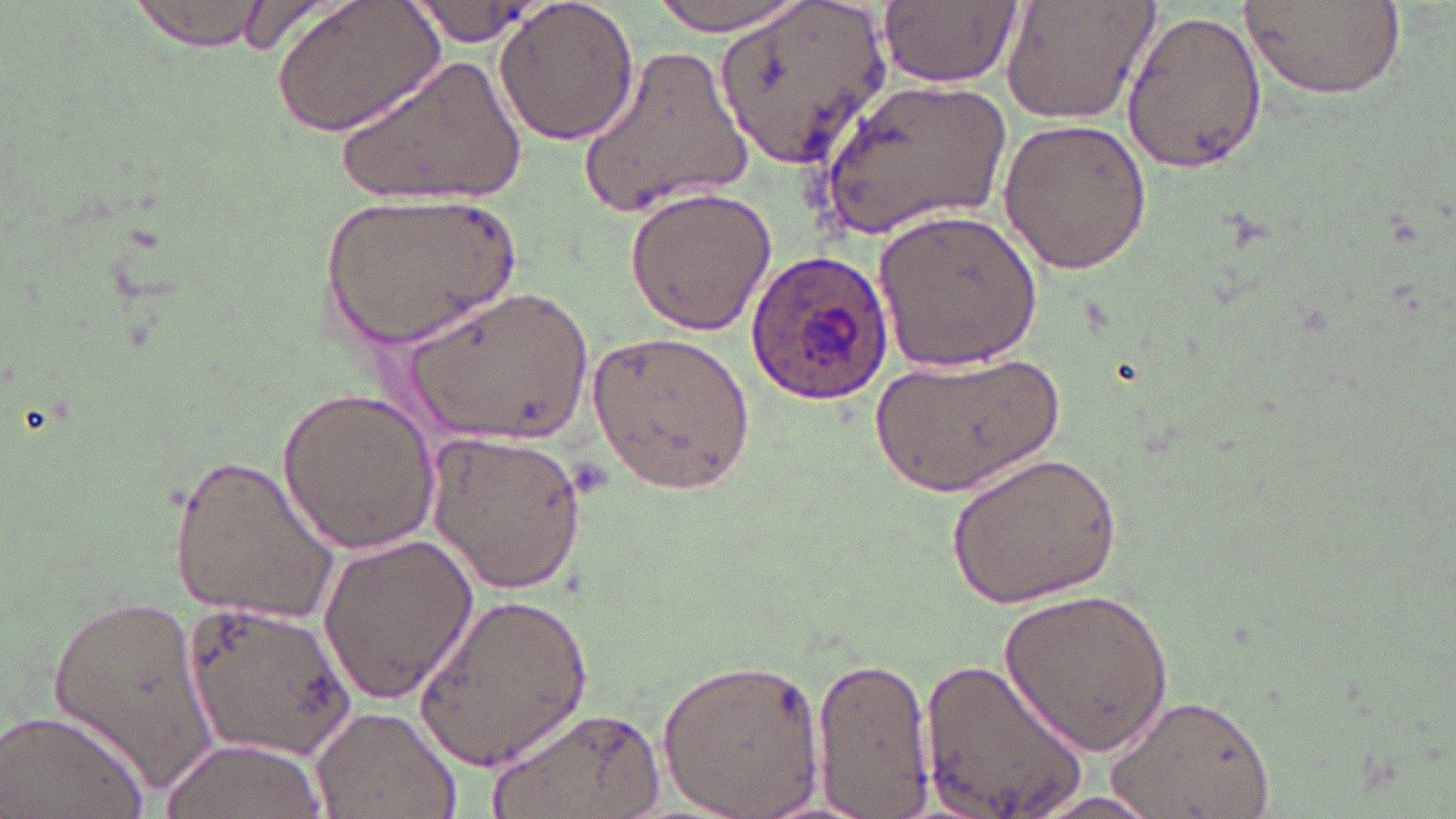

{
  "slide_level_diagnosis": "Plasmodium ovale",
  "uninfected_red_blood_cell_locations": "approximate bounding boxes as (x1,y1)-(x2,y2) corner pairs in pixels: (129,0)-(268,53), (272,0)-(446,139), (495,0)-(640,148), (648,0)-(811,35), (714,0)-(889,170), (1001,0)-(1162,125), (1235,0)-(1407,100), (405,1)-(541,50), (880,1)-(1020,89), (1121,6)-(1270,174), (577,45)-(755,218), (341,51)-(526,209), (816,76)-(1016,238), (996,117)-(1152,276), (625,186)-(778,335), (321,190)-(520,350), (873,207)-(1044,372), (408,283)-(592,443), (584,326)-(754,497), (866,349)-(1062,495), (276,387)-(446,553), (419,429)-(592,595), (948,448)-(1123,608), (171,449)-(342,627), (314,533)-(482,704), (1001,585)-(1179,757), (413,590)-(593,773), (49,592)-(224,792), (183,597)-(359,763), (809,652)-(933,815), (920,652)-(1092,819), (655,655)-(826,817), (1105,692)-(1277,819), (489,699)-(665,819), (311,705)-(460,819), (0,706)-(154,819), (159,738)-(326,819), (1025,791)-(1172,818)",
  "plasmodium_ovale_infected_red_blood_cell_locations": "approximate bounding boxes as (x1,y1)-(x2,y2) corner pairs in pixels: (744,248)-(895,407)",
  "magnification": "1000x",
  "preparation": "thin blood smear",
  "image_size": "1456×819 pixels",
  "modality": "light microscopy",
  "stain": "May-Grünwald-Giemsa",
  "field_of_view": "one of a larger specimen"
}